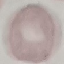

Malaria status: uninfected. Giemsa-stained preparation. Cell patch, automatically extracted from a larger field of view and resized to 64 × 64 pixels. Acquired by smartphone through the microscope eyepiece. Thin smear of blood.